Comment on the morphology of the erythrocytes.
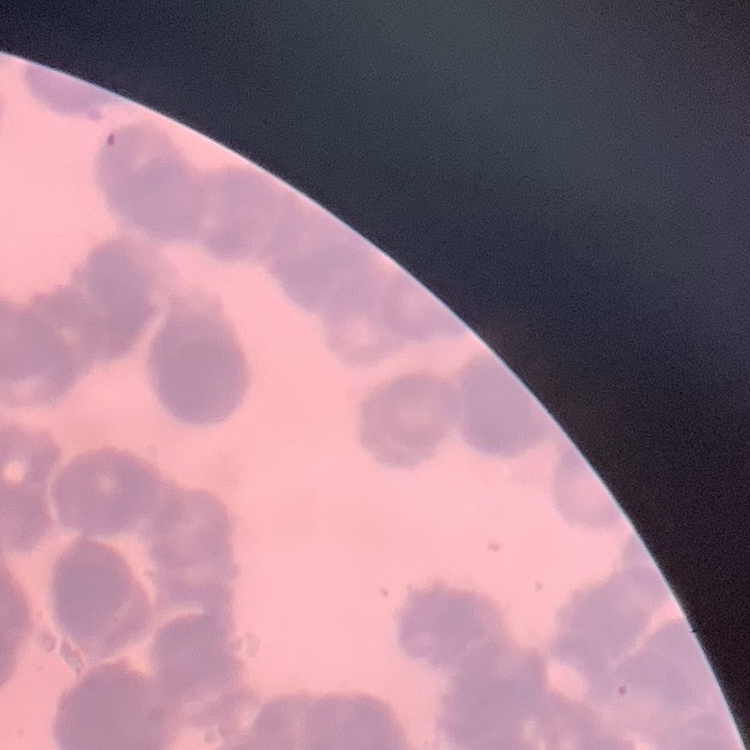
They show rouleaux formation.

image_type: one tile cut from a larger photomicrograph
preparation: thin blood smear
stain: Field's or Giemsa